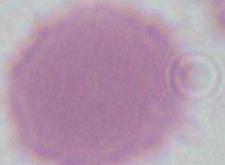
Summary:
  - Magnification: 1000x
  - Identification: erythrocyte
  - Modality: photomicrograph